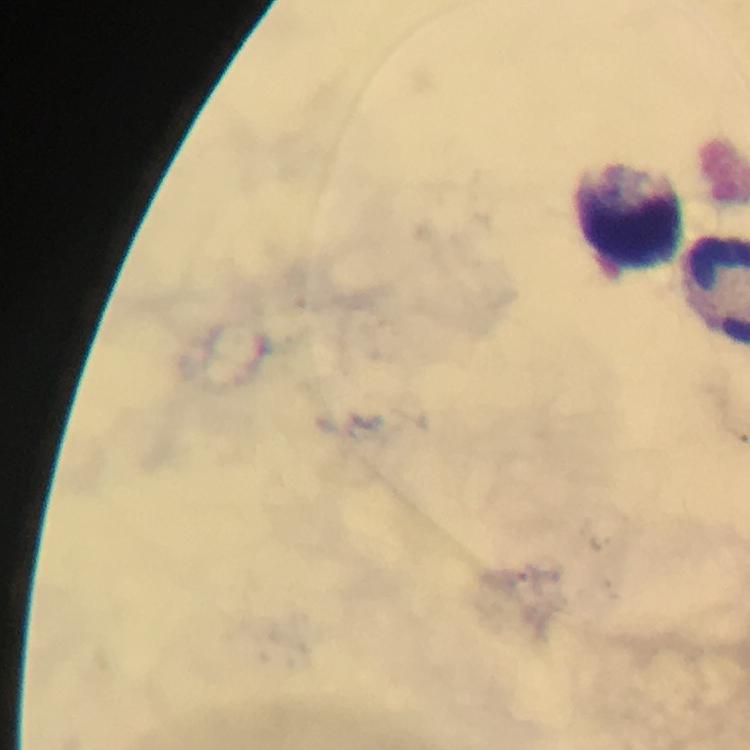
capture = smartphone camera through the microscope
image size = 750×750 pixels
preparation = thick blood film
stain = Giemsa
immersion oil = used
cropped from = one field of view
malaria parasites = none seen
magnification = 100x
context = from a malaria diagnostic workup
leukocyte locations = approximate centers as (x, y) in pixels: (629, 210)